State which cell type is depicted.
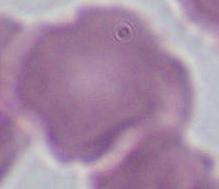

This is an erythrocyte.

magnification = 1000x
modality = micrograph